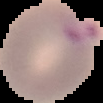
image size = 103×103 pixels
preparation = thin blood film
malaria status = parasitized
image type = segmented cell region on a black background